Assess this cell for malaria.
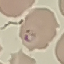
It is parasitized.

Acquired by smartphone through the microscope eyepiece. Automatically extracted cell patch, resized to 64 × 64 pixels. Giemsa-stained preparation. Thin blood smear.